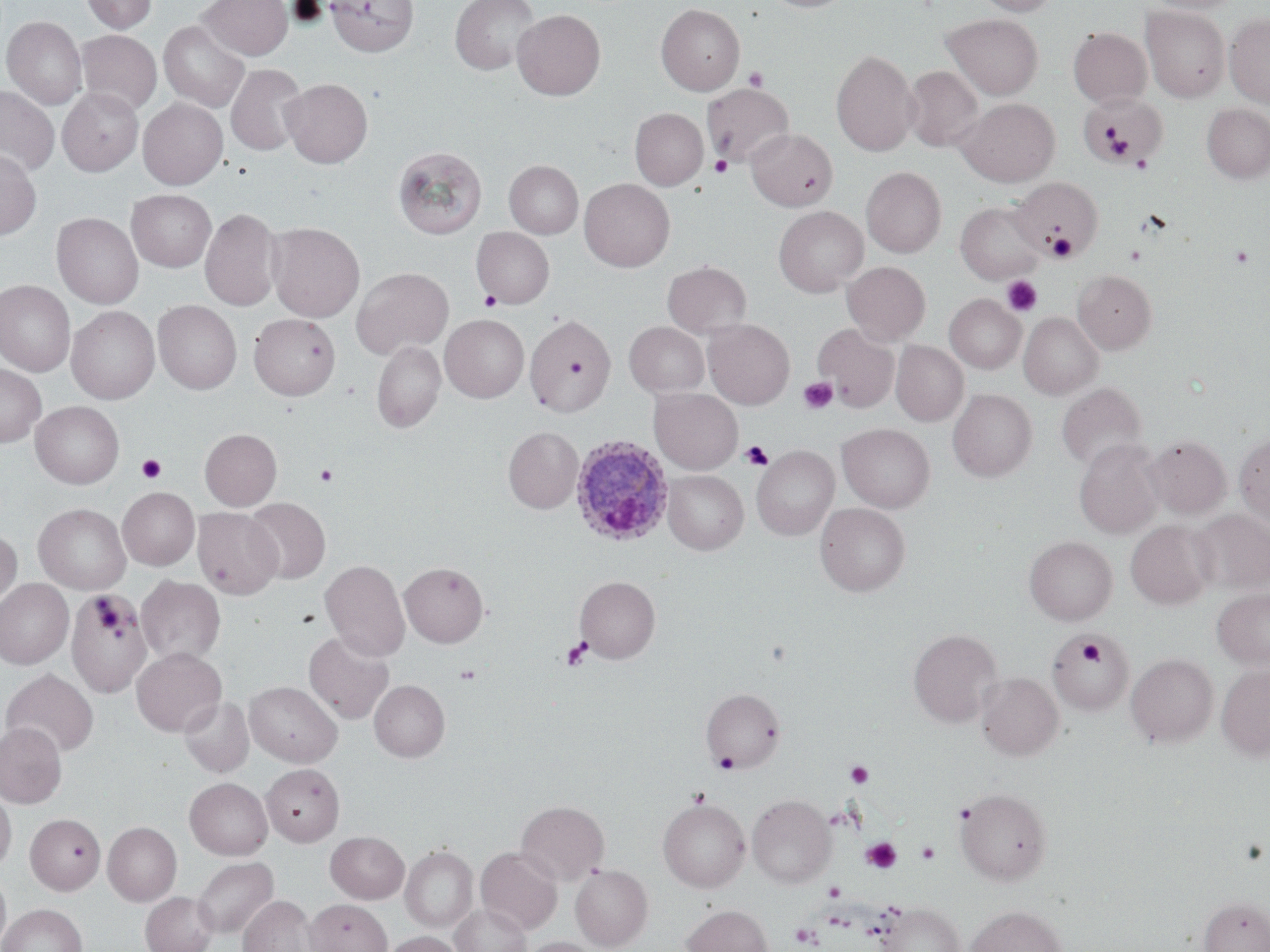

Plasmodium ovale-infected red blood cell locations = approximate bounding boxes as named x1/y1/x2/y2 corners in pixels: (x1=570, y1=436, x2=673, y2=547)
slide-level diagnosis = Plasmodium ovale
platelet locations = approximate bounding boxes as named x1/y1/x2/y2 corners in pixels: (x1=744, y1=67, x2=769, y2=91), (x1=1080, y1=95, x2=1163, y2=165), (x1=1102, y1=126, x2=1136, y2=162), (x1=710, y1=155, x2=732, y2=177), (x1=1130, y1=155, x2=1153, y2=174), (x1=1047, y1=233, x2=1077, y2=261), (x1=1231, y1=244, x2=1255, y2=268), (x1=1002, y1=275, x2=1042, y2=316), (x1=480, y1=290, x2=501, y2=311), (x1=798, y1=377, x2=838, y2=414), (x1=740, y1=441, x2=774, y2=471), (x1=137, y1=454, x2=166, y2=484), (x1=315, y1=464, x2=337, y2=486), (x1=96, y1=598, x2=112, y2=613), (x1=101, y1=611, x2=118, y2=628), (x1=113, y1=628, x2=125, y2=642), (x1=561, y1=637, x2=592, y2=670), (x1=1077, y1=639, x2=1104, y2=667), (x1=455, y1=664, x2=481, y2=685), (x1=713, y1=753, x2=739, y2=774), (x1=846, y1=761, x2=874, y2=787), (x1=689, y1=787, x2=711, y2=806), (x1=861, y1=837, x2=901, y2=874), (x1=916, y1=841, x2=940, y2=864), (x1=824, y1=881, x2=844, y2=901), (x1=791, y1=923, x2=820, y2=947)
preparation = thin blood smear
stain = May-Grünwald-Giemsa
field of view = one of a larger specimen
magnification = 1000x
uninfected red blood cell locations = approximate bounding boxes as named x1/y1/x2/y2 corners in pixels: (x1=81, y1=0, x2=157, y2=33), (x1=199, y1=0, x2=292, y2=59), (x1=326, y1=0, x2=419, y2=56), (x1=450, y1=0, x2=539, y2=75), (x1=762, y1=0, x2=854, y2=13), (x1=972, y1=0, x2=1058, y2=15), (x1=1146, y1=0, x2=1242, y2=14), (x1=656, y1=4, x2=744, y2=95), (x1=1141, y1=5, x2=1230, y2=102), (x1=512, y1=9, x2=606, y2=100), (x1=943, y1=14, x2=1043, y2=99), (x1=1225, y1=14, x2=1270, y2=108), (x1=2, y1=16, x2=87, y2=110), (x1=159, y1=20, x2=249, y2=112), (x1=1068, y1=27, x2=1151, y2=107), (x1=76, y1=30, x2=162, y2=116), (x1=831, y1=49, x2=919, y2=156), (x1=226, y1=64, x2=308, y2=156), (x1=903, y1=66, x2=983, y2=152), (x1=281, y1=78, x2=372, y2=167), (x1=702, y1=84, x2=795, y2=167), (x1=0, y1=85, x2=59, y2=177), (x1=58, y1=87, x2=143, y2=176), (x1=1080, y1=92, x2=1164, y2=166), (x1=138, y1=98, x2=228, y2=189), (x1=956, y1=98, x2=1060, y2=186), (x1=1202, y1=103, x2=1270, y2=183), (x1=631, y1=109, x2=708, y2=190), (x1=746, y1=129, x2=837, y2=211), (x1=393, y1=145, x2=486, y2=239), (x1=0, y1=149, x2=41, y2=240), (x1=504, y1=160, x2=583, y2=238), (x1=862, y1=167, x2=946, y2=257), (x1=580, y1=178, x2=674, y2=271), (x1=1012, y1=178, x2=1102, y2=258), (x1=127, y1=190, x2=216, y2=272), (x1=956, y1=202, x2=1044, y2=283), (x1=774, y1=206, x2=868, y2=297), (x1=200, y1=207, x2=282, y2=311), (x1=52, y1=212, x2=143, y2=308), (x1=267, y1=222, x2=364, y2=322), (x1=471, y1=227, x2=554, y2=308), (x1=663, y1=261, x2=751, y2=338), (x1=842, y1=261, x2=930, y2=345), (x1=352, y1=266, x2=453, y2=359), (x1=1073, y1=270, x2=1156, y2=353), (x1=0, y1=280, x2=75, y2=375), (x1=945, y1=294, x2=1025, y2=373), (x1=153, y1=300, x2=241, y2=394), (x1=66, y1=306, x2=160, y2=404), (x1=1020, y1=312, x2=1102, y2=399), (x1=249, y1=314, x2=340, y2=400), (x1=441, y1=314, x2=528, y2=402), (x1=525, y1=314, x2=615, y2=416), (x1=703, y1=319, x2=794, y2=409), (x1=624, y1=322, x2=709, y2=397), (x1=813, y1=324, x2=899, y2=411), (x1=372, y1=341, x2=445, y2=432), (x1=891, y1=341, x2=968, y2=426), (x1=0, y1=364, x2=46, y2=446), (x1=1057, y1=383, x2=1147, y2=471), (x1=649, y1=388, x2=743, y2=474), (x1=948, y1=389, x2=1037, y2=481), (x1=31, y1=401, x2=124, y2=489), (x1=837, y1=423, x2=935, y2=512), (x1=503, y1=427, x2=583, y2=513), (x1=200, y1=428, x2=282, y2=510), (x1=1234, y1=433, x2=1270, y2=528), (x1=1143, y1=435, x2=1231, y2=519), (x1=1074, y1=439, x2=1164, y2=538), (x1=752, y1=445, x2=838, y2=539), (x1=663, y1=470, x2=747, y2=554), (x1=117, y1=487, x2=199, y2=570), (x1=244, y1=498, x2=330, y2=583), (x1=34, y1=503, x2=131, y2=594), (x1=816, y1=503, x2=910, y2=596), (x1=192, y1=508, x2=282, y2=599), (x1=1191, y1=508, x2=1270, y2=595), (x1=1125, y1=519, x2=1216, y2=609), (x1=0, y1=530, x2=22, y2=608), (x1=1024, y1=536, x2=1117, y2=625), (x1=320, y1=559, x2=409, y2=660), (x1=400, y1=562, x2=488, y2=647), (x1=137, y1=576, x2=226, y2=666), (x1=575, y1=576, x2=660, y2=662), (x1=0, y1=579, x2=73, y2=669), (x1=1212, y1=587, x2=1270, y2=670), (x1=66, y1=589, x2=152, y2=698), (x1=908, y1=628, x2=1002, y2=727), (x1=1047, y1=630, x2=1135, y2=716), (x1=304, y1=631, x2=394, y2=724), (x1=131, y1=647, x2=226, y2=736), (x1=1126, y1=654, x2=1218, y2=747), (x1=1217, y1=664, x2=1270, y2=760), (x1=2, y1=669, x2=99, y2=758), (x1=976, y1=672, x2=1063, y2=760), (x1=369, y1=680, x2=449, y2=761), (x1=245, y1=681, x2=342, y2=766), (x1=701, y1=687, x2=785, y2=773), (x1=179, y1=696, x2=254, y2=778), (x1=0, y1=722, x2=67, y2=808), (x1=262, y1=763, x2=344, y2=846), (x1=185, y1=777, x2=272, y2=859), (x1=955, y1=787, x2=1052, y2=884), (x1=0, y1=790, x2=15, y2=873), (x1=747, y1=794, x2=835, y2=887), (x1=658, y1=798, x2=749, y2=891), (x1=516, y1=800, x2=609, y2=885), (x1=25, y1=813, x2=105, y2=894), (x1=103, y1=822, x2=181, y2=905), (x1=326, y1=831, x2=409, y2=903), (x1=400, y1=845, x2=477, y2=932), (x1=475, y1=846, x2=562, y2=934), (x1=192, y1=857, x2=278, y2=938), (x1=570, y1=864, x2=653, y2=951), (x1=0, y1=871, x2=11, y2=951), (x1=140, y1=891, x2=218, y2=952), (x1=239, y1=895, x2=317, y2=952), (x1=1199, y1=897, x2=1270, y2=952), (x1=305, y1=898, x2=392, y2=952), (x1=0, y1=903, x2=87, y2=952), (x1=450, y1=903, x2=530, y2=952), (x1=879, y1=903, x2=965, y2=952), (x1=682, y1=904, x2=772, y2=952), (x1=966, y1=905, x2=1066, y2=952), (x1=384, y1=931, x2=464, y2=952), (x1=520, y1=937, x2=604, y2=952)
modality = optical microscopy
image size = 1270×952 pixels